Point out Plasmodium parasites and leukocytes.
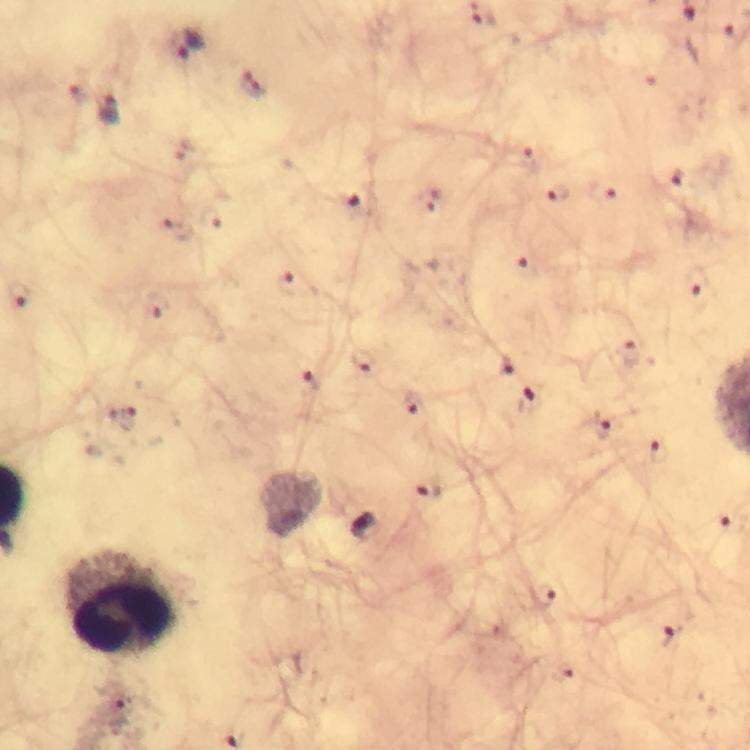
Approximate centers as [x, y] in pixels.
Plasmodium parasites: [689, 19], [191, 49], [253, 85], [75, 93], [112, 108], [525, 157], [682, 180], [603, 189], [560, 194], [435, 203], [357, 205], [173, 230], [522, 269], [288, 282], [697, 286], [24, 295], [155, 306], [628, 354], [361, 361], [505, 365], [310, 383], [531, 401], [413, 404], [126, 419], [602, 424], [661, 452], [428, 488], [732, 521], [541, 597], [674, 635].
Leukocytes: [123, 604].

Summary:
  - Immersion oil: used
  - Capture: smartphone mounted on the microscope
  - Cropped from: a single field of view
  - Image size: 750×750 pixels
  - Stain: Giemsa
  - Magnification: 100x
  - Context: from a malaria diagnostic workup
  - Preparation: thick smear